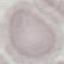

Result: no malaria parasites seen. Thin blood film. Automatically extracted cell patch, resized to 64 × 64 pixels. Giemsa stain. Photographed with a smartphone camera at the microscope eyepiece.